Point out each malaria parasite.
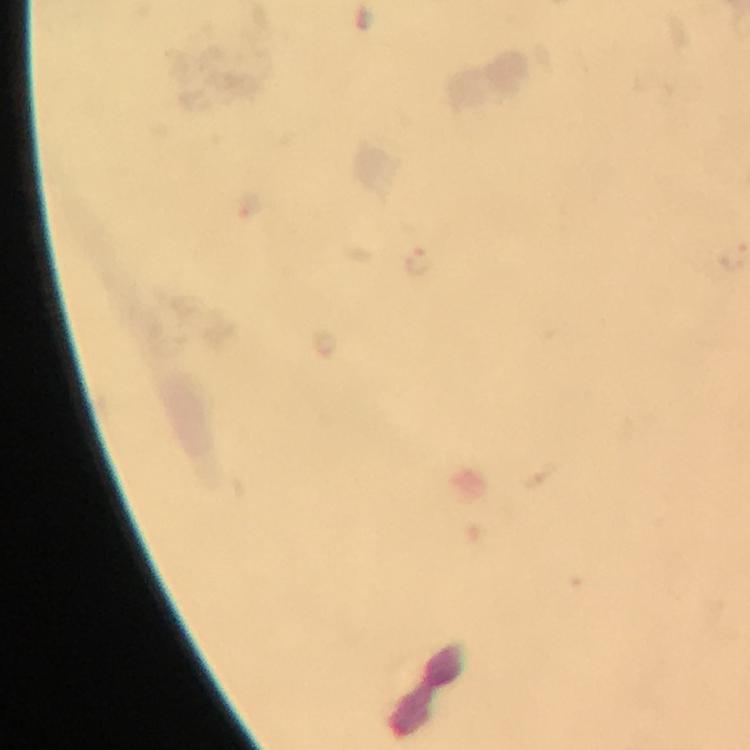
Approximate object centers, in pixels from the top-left corner.
Malaria parasites: (x=417, y=259).

Thick blood smear. 100x magnification. Immersion oil applied. Cropped region of a single field of view. Photographed with a smartphone mounted on the microscope. From a diagnostic examination for malaria. Image is 750×750 pixels. Giemsa stain.